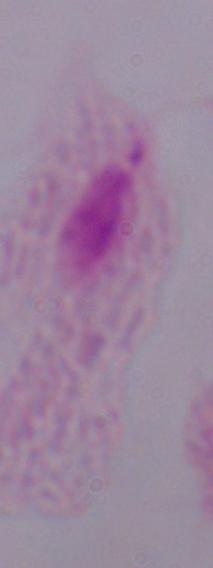 Photomicrograph. A trichomonad is seen. Captured at 1000x magnification.